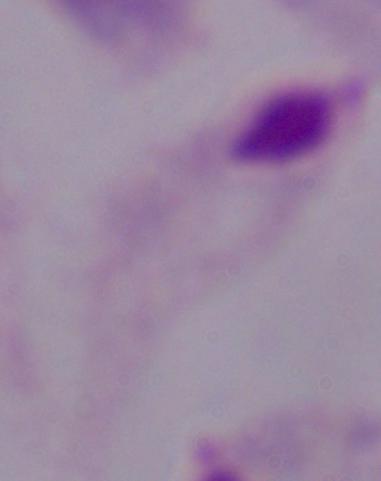
Summary:
  - Identification: trichomonad
  - Modality: micrograph
  - Magnification: 1000x